State the blood parasite species.
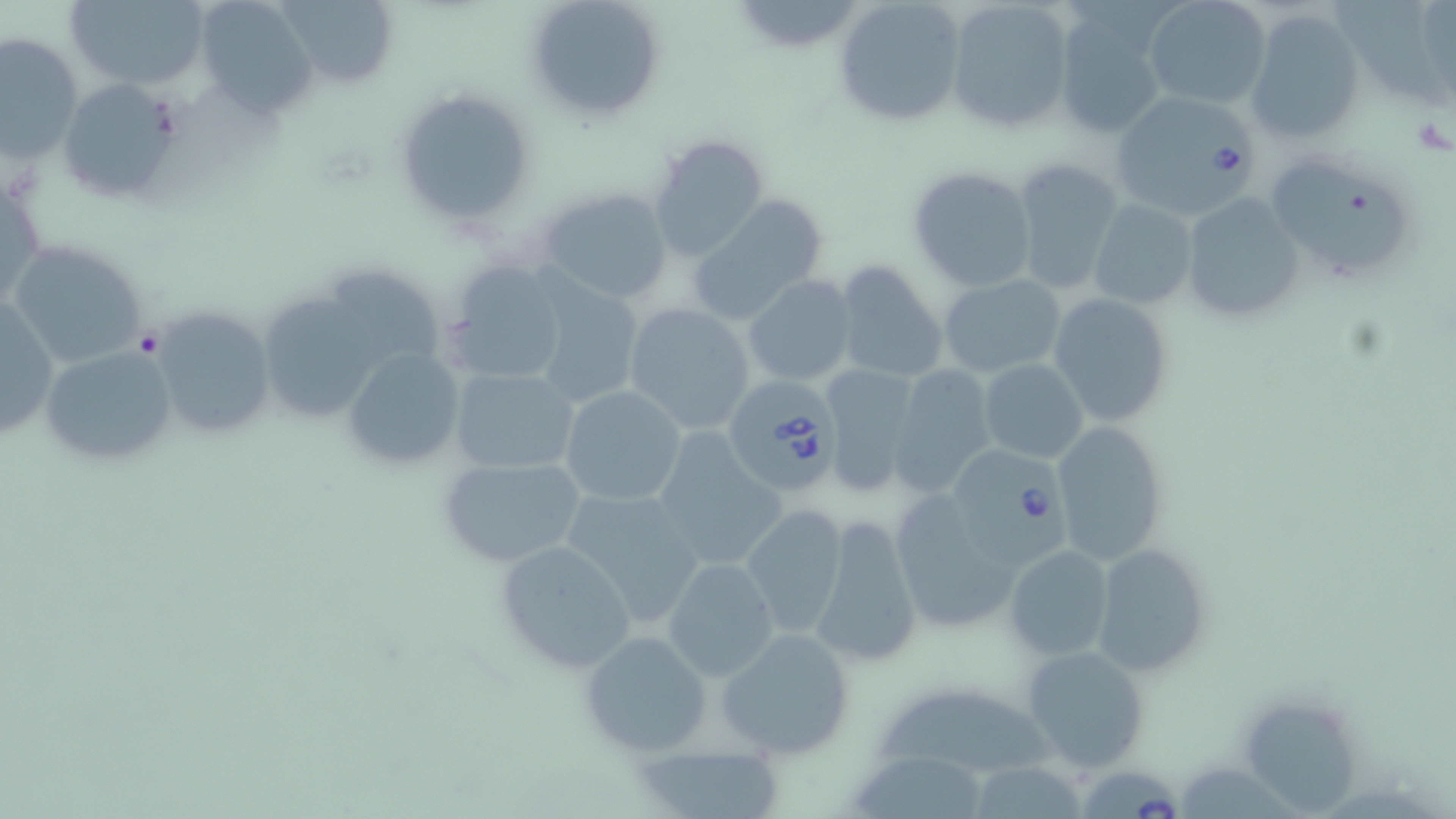
Babesia divergens.

Summary:
  - Coordinate format: approximate bounding boxes as named x1/y1/x2/y2 corners in pixels
  - Uninfected red blood cell locations: (x1=64, y1=0, x2=210, y2=91), (x1=195, y1=0, x2=319, y2=116), (x1=277, y1=0, x2=400, y2=90), (x1=523, y1=0, x2=666, y2=122), (x1=742, y1=0, x2=864, y2=49), (x1=835, y1=0, x2=965, y2=126), (x1=943, y1=0, x2=1073, y2=135), (x1=1143, y1=0, x2=1273, y2=111), (x1=1342, y1=2, x2=1453, y2=119), (x1=1054, y1=8, x2=1173, y2=141), (x1=1244, y1=9, x2=1366, y2=147), (x1=1, y1=31, x2=83, y2=164), (x1=57, y1=77, x2=183, y2=203), (x1=394, y1=89, x2=537, y2=226), (x1=649, y1=134, x2=771, y2=263), (x1=1263, y1=154, x2=1414, y2=286), (x1=1010, y1=158, x2=1124, y2=297), (x1=907, y1=164, x2=1039, y2=293), (x1=1, y1=169, x2=46, y2=316), (x1=535, y1=185, x2=673, y2=305), (x1=1180, y1=192, x2=1306, y2=324), (x1=687, y1=197, x2=830, y2=325), (x1=1087, y1=199, x2=1197, y2=310), (x1=6, y1=239, x2=152, y2=371), (x1=833, y1=258, x2=950, y2=386), (x1=442, y1=259, x2=571, y2=389), (x1=313, y1=263, x2=447, y2=369), (x1=742, y1=275, x2=857, y2=387), (x1=940, y1=275, x2=1066, y2=379), (x1=530, y1=281, x2=644, y2=411), (x1=1047, y1=291, x2=1175, y2=428), (x1=1, y1=294, x2=60, y2=445), (x1=259, y1=300, x2=383, y2=413), (x1=623, y1=303, x2=758, y2=434), (x1=146, y1=307, x2=277, y2=445), (x1=40, y1=343, x2=178, y2=470), (x1=340, y1=347, x2=470, y2=475), (x1=979, y1=358, x2=1089, y2=463), (x1=449, y1=364, x2=581, y2=475), (x1=817, y1=364, x2=925, y2=497), (x1=887, y1=364, x2=998, y2=498), (x1=558, y1=384, x2=687, y2=507), (x1=1049, y1=419, x2=1169, y2=564), (x1=650, y1=430, x2=785, y2=573), (x1=436, y1=454, x2=589, y2=570), (x1=559, y1=486, x2=706, y2=630), (x1=887, y1=489, x2=1028, y2=637), (x1=740, y1=506, x2=849, y2=640), (x1=810, y1=513, x2=922, y2=669), (x1=496, y1=540, x2=636, y2=673), (x1=1091, y1=541, x2=1211, y2=676), (x1=1005, y1=545, x2=1115, y2=661), (x1=662, y1=557, x2=779, y2=682), (x1=718, y1=628, x2=855, y2=758), (x1=579, y1=630, x2=711, y2=757), (x1=1020, y1=644, x2=1149, y2=773), (x1=874, y1=689, x2=1058, y2=773), (x1=1246, y1=703, x2=1360, y2=814), (x1=632, y1=743, x2=788, y2=817), (x1=852, y1=753, x2=983, y2=819), (x1=964, y1=761, x2=1093, y2=817), (x1=1180, y1=765, x2=1298, y2=819)
  - Babesia divergens-infected red blood cell locations: (x1=1107, y1=91, x2=1260, y2=219), (x1=725, y1=376, x2=844, y2=497), (x1=946, y1=446, x2=1071, y2=573), (x1=1085, y1=769, x2=1182, y2=819)
  - Platelet locations: (x1=135, y1=328, x2=164, y2=357)
  - Image size: 1456×819 pixels
  - Stain: May-Grünwald-Giemsa
  - Magnification: 1000x
  - Modality: light microscopy
  - Preparation: thin blood smear
  - Field of view: single